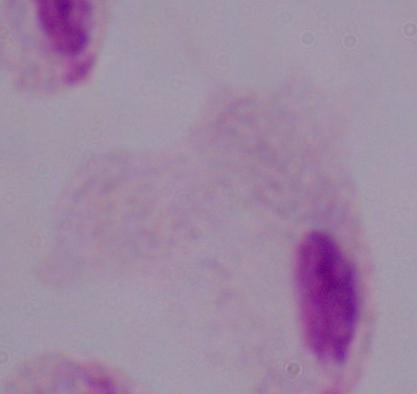

Summary:
  - Modality: photomicrograph
  - Magnification: 1000x
  - Identification: trichomonad